Classify this cell by malaria status.
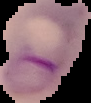
It is parasitized.

From a thin blood smear. The area outside the segmented cell region is set to black. Image is 91×103 pixels.